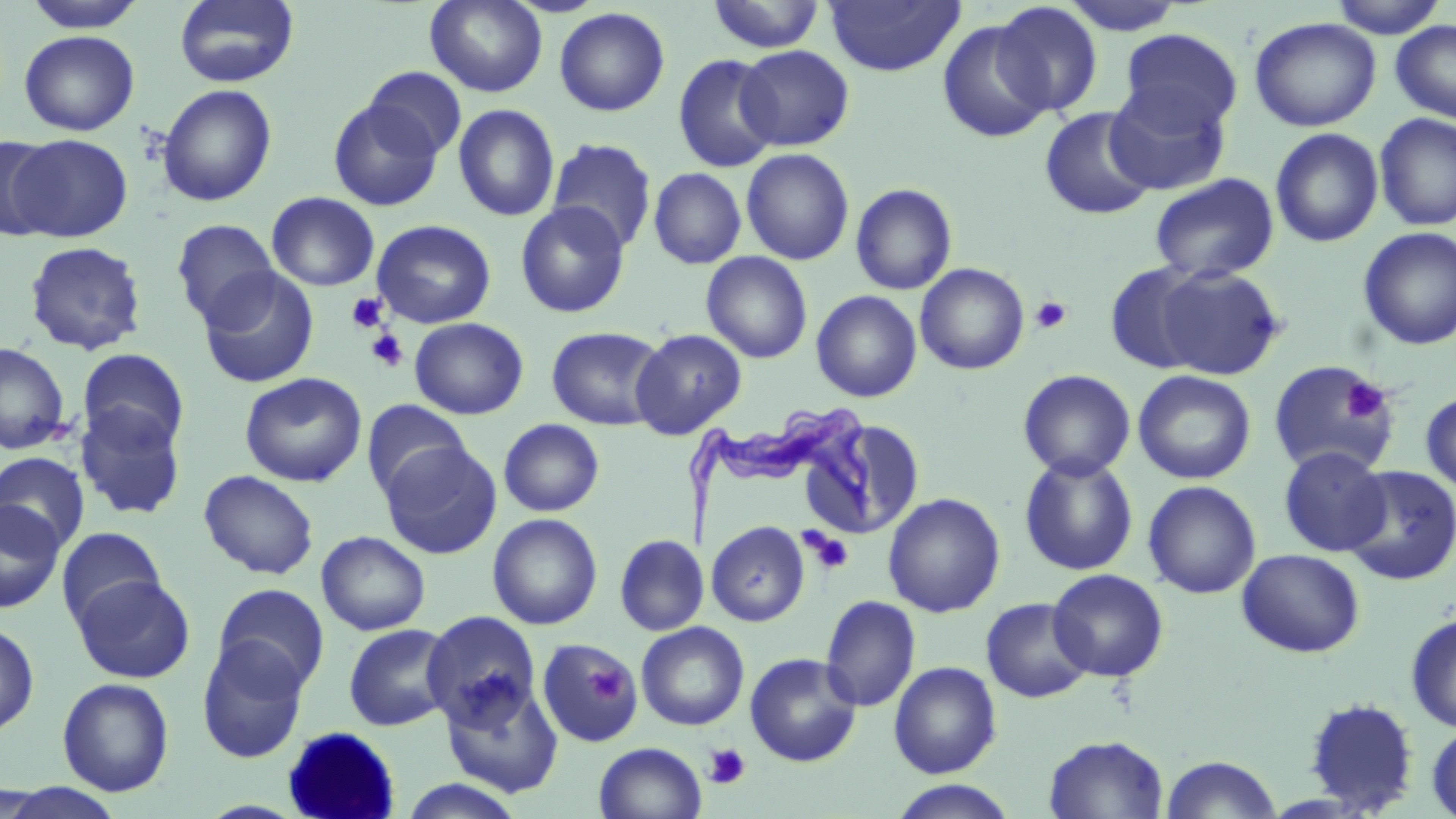
Summary:
  - Coordinate format: approximate bounding boxes as named x1/y1/x2/y2 corners in pixels
  - Uninfected red blood cell locations: (x1=22, y1=0, x2=149, y2=33), (x1=173, y1=0, x2=299, y2=88), (x1=1059, y1=0, x2=1188, y2=36), (x1=1326, y1=0, x2=1448, y2=39), (x1=425, y1=1, x2=548, y2=97), (x1=706, y1=1, x2=826, y2=53), (x1=824, y1=1, x2=965, y2=77), (x1=989, y1=2, x2=1104, y2=117), (x1=554, y1=7, x2=670, y2=116), (x1=1249, y1=17, x2=1382, y2=132), (x1=936, y1=19, x2=1054, y2=144), (x1=1390, y1=19, x2=1456, y2=125), (x1=1118, y1=28, x2=1243, y2=135), (x1=19, y1=30, x2=139, y2=136), (x1=735, y1=45, x2=855, y2=151), (x1=672, y1=53, x2=782, y2=174), (x1=364, y1=66, x2=467, y2=158), (x1=1104, y1=82, x2=1233, y2=195), (x1=157, y1=83, x2=277, y2=207), (x1=328, y1=98, x2=443, y2=212), (x1=453, y1=103, x2=560, y2=222), (x1=1039, y1=106, x2=1156, y2=220), (x1=1375, y1=113, x2=1456, y2=232), (x1=1270, y1=127, x2=1384, y2=248), (x1=7, y1=134, x2=132, y2=242), (x1=0, y1=135, x2=61, y2=241), (x1=547, y1=138, x2=657, y2=252), (x1=740, y1=148, x2=855, y2=266), (x1=648, y1=167, x2=747, y2=269), (x1=1150, y1=173, x2=1280, y2=283), (x1=850, y1=183, x2=958, y2=296), (x1=266, y1=191, x2=379, y2=291), (x1=515, y1=201, x2=631, y2=319), (x1=170, y1=219, x2=280, y2=326), (x1=371, y1=219, x2=496, y2=329), (x1=1357, y1=227, x2=1456, y2=350), (x1=24, y1=240, x2=148, y2=356), (x1=701, y1=251, x2=813, y2=363), (x1=915, y1=263, x2=1029, y2=375), (x1=1104, y1=263, x2=1212, y2=374), (x1=1153, y1=263, x2=1287, y2=380), (x1=197, y1=267, x2=319, y2=389), (x1=811, y1=290, x2=922, y2=402), (x1=409, y1=317, x2=529, y2=420), (x1=546, y1=326, x2=667, y2=430), (x1=631, y1=329, x2=747, y2=439), (x1=0, y1=341, x2=71, y2=455), (x1=77, y1=348, x2=189, y2=452), (x1=1267, y1=360, x2=1396, y2=477), (x1=1017, y1=369, x2=1136, y2=480), (x1=1133, y1=370, x2=1256, y2=485), (x1=240, y1=372, x2=367, y2=487), (x1=1420, y1=391, x2=1456, y2=495), (x1=362, y1=400, x2=471, y2=500), (x1=76, y1=402, x2=187, y2=520), (x1=498, y1=418, x2=604, y2=517), (x1=801, y1=419, x2=927, y2=540), (x1=380, y1=441, x2=501, y2=559), (x1=1278, y1=445, x2=1391, y2=556), (x1=0, y1=451, x2=90, y2=554), (x1=1019, y1=454, x2=1138, y2=577), (x1=1341, y1=465, x2=1456, y2=586), (x1=199, y1=470, x2=319, y2=580), (x1=1143, y1=480, x2=1262, y2=599), (x1=883, y1=493, x2=1005, y2=618), (x1=0, y1=499, x2=65, y2=614), (x1=487, y1=513, x2=603, y2=630), (x1=705, y1=521, x2=810, y2=627), (x1=57, y1=526, x2=167, y2=629), (x1=316, y1=530, x2=431, y2=635), (x1=614, y1=533, x2=708, y2=636), (x1=1236, y1=548, x2=1365, y2=657), (x1=1048, y1=568, x2=1169, y2=682), (x1=73, y1=574, x2=195, y2=683), (x1=213, y1=584, x2=330, y2=693), (x1=820, y1=595, x2=921, y2=712), (x1=981, y1=597, x2=1094, y2=703), (x1=422, y1=611, x2=542, y2=729), (x1=1405, y1=612, x2=1456, y2=734), (x1=0, y1=621, x2=39, y2=737), (x1=636, y1=621, x2=749, y2=730), (x1=343, y1=623, x2=457, y2=732), (x1=196, y1=637, x2=310, y2=763), (x1=537, y1=637, x2=643, y2=747), (x1=744, y1=652, x2=862, y2=767), (x1=888, y1=661, x2=1002, y2=778), (x1=57, y1=677, x2=174, y2=796), (x1=439, y1=677, x2=564, y2=799), (x1=1301, y1=698, x2=1420, y2=814), (x1=1426, y1=722, x2=1456, y2=819), (x1=1042, y1=734, x2=1169, y2=818), (x1=594, y1=741, x2=707, y2=819), (x1=1160, y1=754, x2=1282, y2=818), (x1=396, y1=777, x2=530, y2=819), (x1=888, y1=780, x2=1019, y2=818)
  - Platelet locations: (x1=346, y1=293, x2=387, y2=333), (x1=1030, y1=296, x2=1073, y2=334), (x1=365, y1=328, x2=408, y2=372), (x1=1342, y1=378, x2=1388, y2=424), (x1=801, y1=528, x2=854, y2=574), (x1=589, y1=666, x2=629, y2=705), (x1=704, y1=744, x2=751, y2=789)
  - Trypanosoma brucei locations: (x1=680, y1=400, x2=876, y2=547)
  - Slide-level diagnosis: Trypanosoma brucei
  - Magnification: 1000x
  - Field of view: one of a larger specimen
  - Preparation: thin blood film
  - Stain: May-Grünwald-Giemsa
  - Modality: optical microscopy
  - Image size: 1456×819 pixels